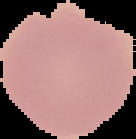

Result: no Plasmodium parasites seen. From a thin blood smear. Cell region segmented out of the field of view; the surrounding area is masked to black. Image is 136×139 pixels.